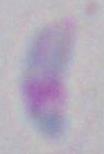
modality = micrograph
magnification = 1000x
identification = Toxoplasma gondii